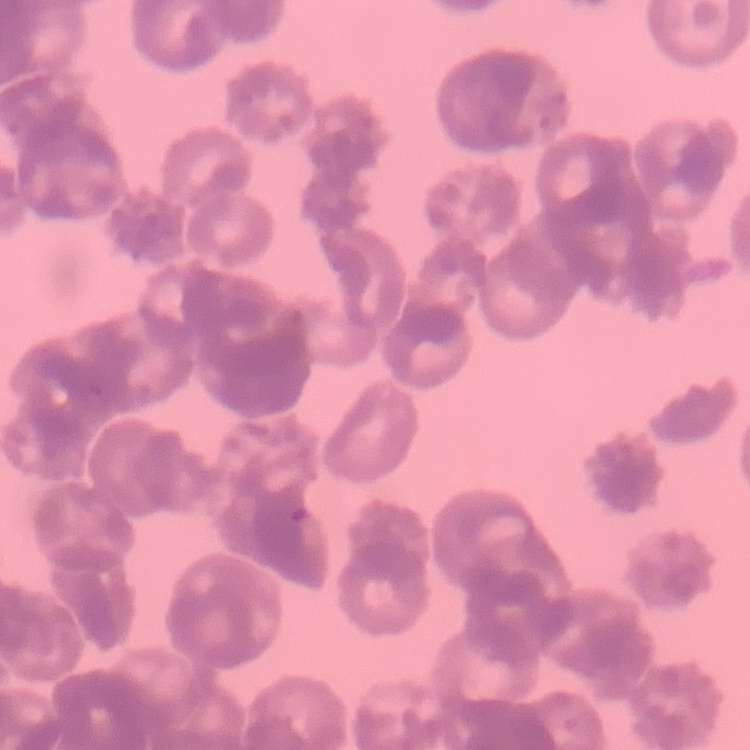

The red blood cells exhibit rouleaux formation. Field's or Giemsa stain. Square crop of a larger photomicrograph. Thin peripheral smear.